Comment on the morphology of the red blood cells.
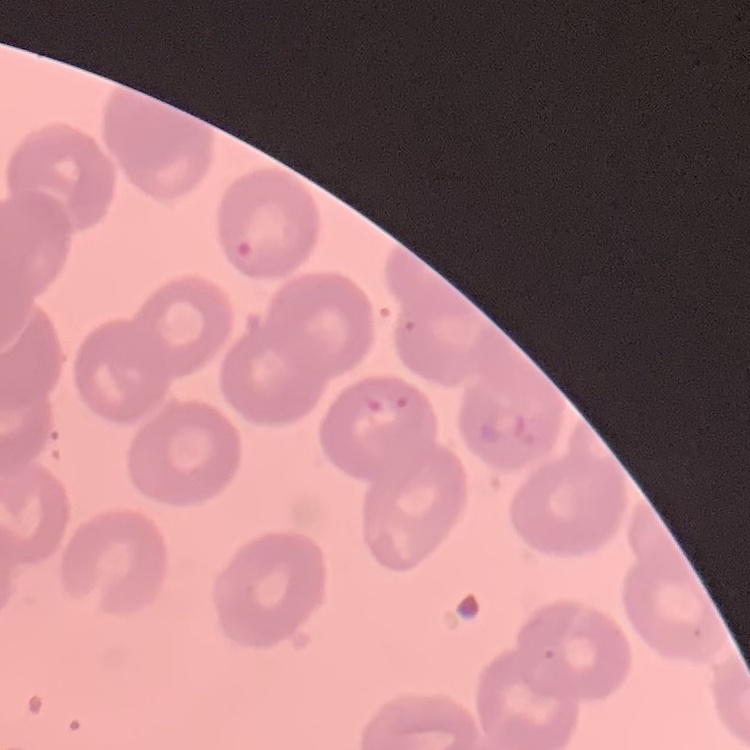

They show no rouleaux formation.

Summary:
  - Image type: one tile cut from a larger photomicrograph
  - Stain: Field's or Giemsa
  - Preparation: thin blood film